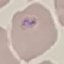
Result: malaria parasites identified. Cell patch, automatically extracted from a larger field of view and resized to 64 × 64 pixels. Thin blood smear. Giemsa-stained preparation. Photographed with a smartphone camera at the microscope eyepiece.